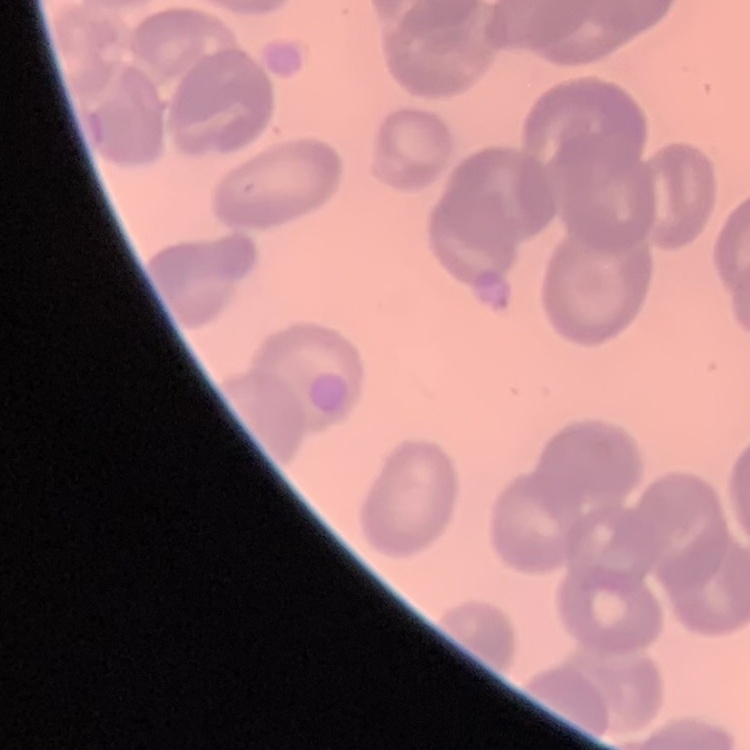
Summary:
  - Erythrocyte morphology: no rouleaux formation
  - Image type: one tile cut from a larger photomicrograph
  - Preparation: thin blood film
  - Stain: Field's or Giemsa